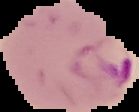

Summary:
  - Result: Plasmodium parasites detected
  - Image type: cell region segmented out of the field of view; surrounding area masked to black
  - Image size: 139×112 pixels
  - Preparation: thin blood smear